Name the parasite shown.
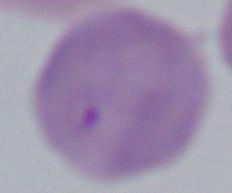
This is Babesia.

Micrograph. Captured at 1000x magnification.